Assess this cell for malaria.
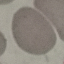
It is uninfected.

stain = Giemsa
image type = automatically extracted cell patch, resized to 64 × 64 pixels
preparation = thin blood smear
capture = smartphone through the microscope eyepiece